Locate and identify every blood parasite.
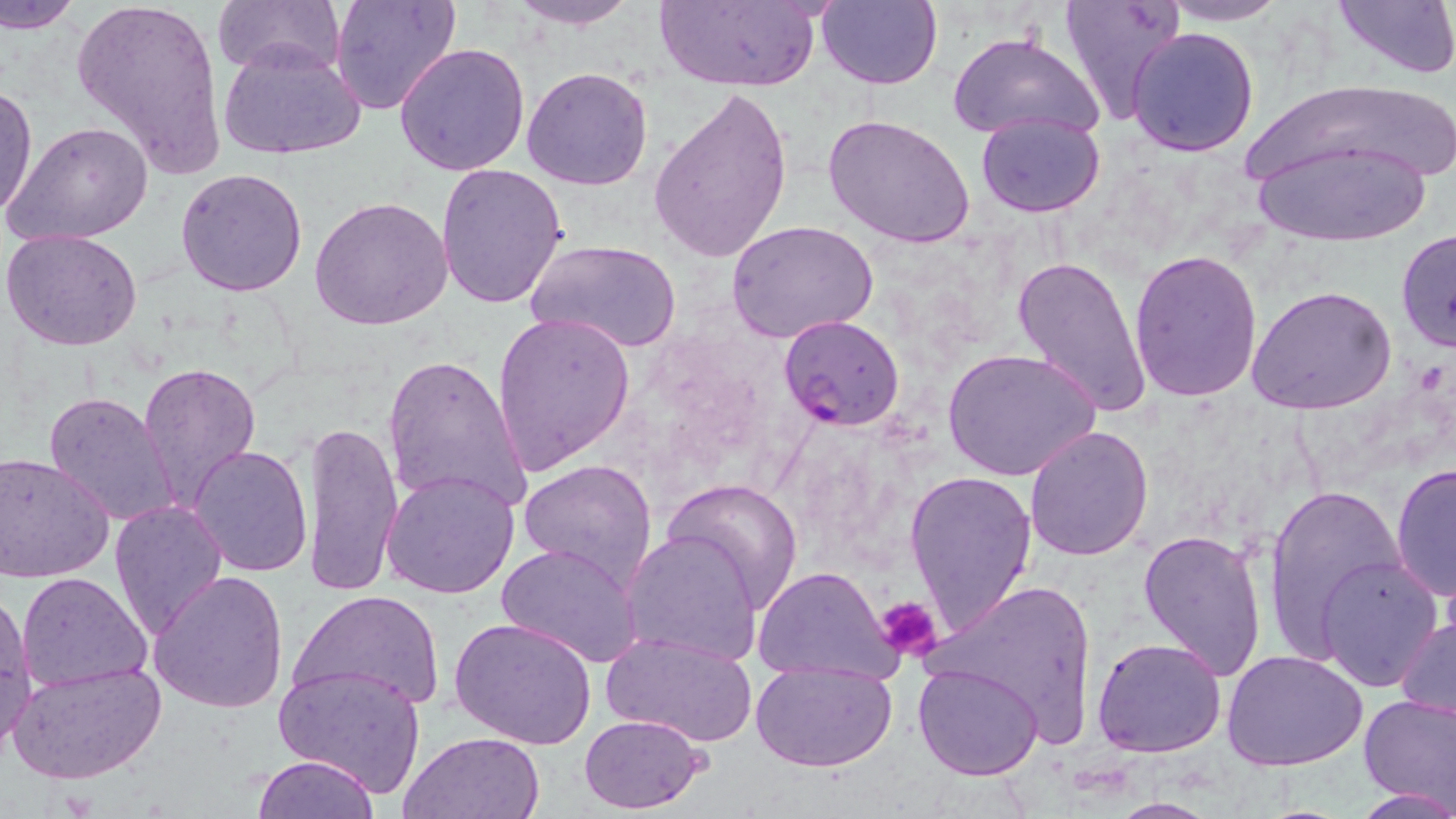

Approximate bounding boxes as (x1, y1, x2, y2) in pixels.
Plasmodium falciparum-infected red blood cells: (779, 314, 905, 431).
No Plasmodium ovale, Plasmodium malariae, Plasmodium vivax, Babesia divergens, or Trypanosoma brucei observed.

Summary:
  - Uninfected red blood cell locations: (2, 0, 84, 33), (71, 0, 229, 182), (213, 0, 346, 78), (328, 0, 460, 116), (507, 0, 642, 29), (653, 0, 820, 89), (819, 0, 943, 90), (1060, 0, 1186, 125), (1331, 0, 1456, 82), (1158, 1, 1291, 25), (1127, 27, 1261, 157), (949, 30, 1105, 147), (218, 41, 366, 160), (395, 43, 532, 177), (522, 65, 654, 191), (1239, 78, 1454, 209), (0, 82, 36, 222), (651, 85, 794, 265), (975, 112, 1106, 218), (823, 113, 975, 250), (10, 122, 153, 245), (1246, 140, 1434, 245), (435, 163, 569, 309), (175, 168, 307, 298), (310, 197, 452, 330), (726, 220, 879, 342), (1395, 227, 1456, 356), (2, 229, 145, 352), (523, 238, 683, 354), (1128, 250, 1263, 402), (1012, 255, 1151, 417), (1247, 284, 1397, 415), (492, 310, 635, 474), (944, 347, 1102, 483), (382, 351, 531, 517), (136, 362, 261, 513), (44, 391, 181, 527), (303, 419, 402, 600), (1023, 424, 1153, 561), (188, 445, 312, 577), (0, 453, 114, 582), (519, 458, 658, 589), (1392, 460, 1456, 603), (902, 467, 1038, 638), (380, 468, 520, 598), (664, 478, 803, 611), (1262, 484, 1407, 661), (108, 501, 227, 640), (1138, 527, 1269, 681), (621, 530, 766, 666), (498, 542, 644, 667), (1317, 553, 1443, 691), (751, 567, 901, 685), (149, 570, 289, 714), (15, 571, 153, 692), (924, 580, 1098, 744), (0, 589, 37, 757), (290, 589, 445, 710), (1395, 612, 1456, 725), (450, 616, 597, 748), (601, 630, 759, 750), (1092, 635, 1226, 757), (1225, 650, 1369, 769), (750, 656, 898, 772), (8, 660, 166, 784), (273, 662, 427, 799), (912, 662, 1044, 780), (1358, 692, 1456, 812), (579, 714, 707, 814), (396, 731, 543, 818), (251, 754, 381, 818), (1352, 788, 1456, 818), (1103, 796, 1220, 817)
  - Platelet locations: (878, 596, 942, 664)
  - Slide-level diagnosis: Plasmodium falciparum
  - Stain: May-Grünwald-Giemsa
  - Field of view: one of a larger specimen
  - Modality: optical microscopy
  - Preparation: thin blood film
  - Magnification: 1000x
  - Image size: 1456×819 pixels